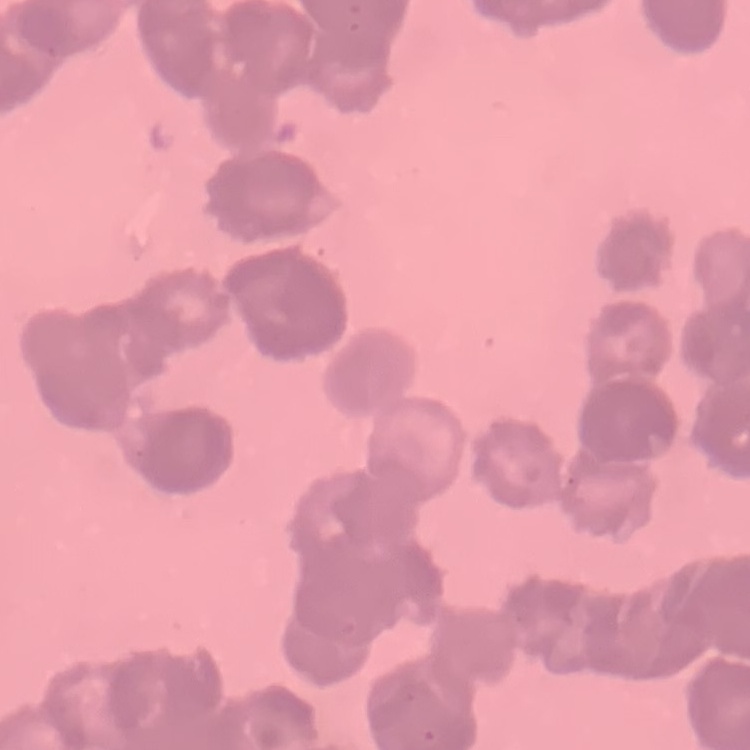
Summary:
  - Erythrocyte morphology: rouleaux formation
  - Preparation: thin blood smear
  - Stain: Field's or Giemsa
  - Image type: one tile cut from a larger photomicrograph